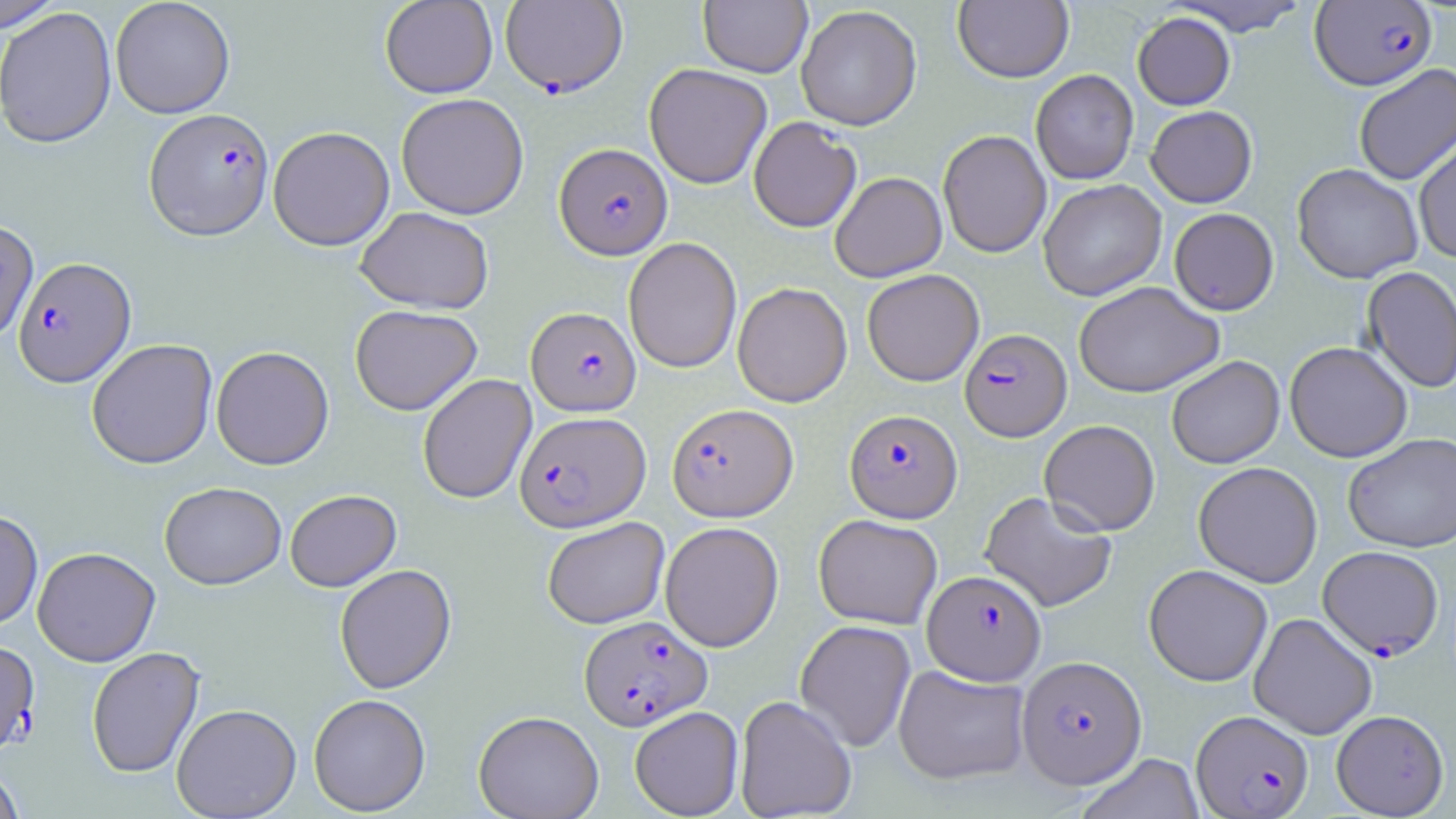

Summary:
  - Coordinate format: approximate bounding boxes as [x1, y1, x2, y2] in pixels
  - Uninfected red blood cell locations: [110, 0, 235, 119], [380, 0, 498, 98], [699, 0, 812, 77], [1166, 0, 1312, 36], [0, 1, 64, 32], [953, 1, 1074, 83], [0, 5, 117, 148], [796, 5, 922, 130], [1132, 11, 1236, 110], [644, 63, 772, 189], [1353, 65, 1456, 186], [1031, 69, 1139, 185], [396, 93, 529, 219], [1145, 105, 1257, 208], [748, 117, 862, 232], [268, 126, 395, 251], [937, 130, 1051, 258], [1414, 135, 1456, 264], [1292, 163, 1423, 284], [829, 171, 947, 282], [1038, 179, 1166, 301], [355, 206, 494, 314], [1169, 208, 1279, 315], [0, 219, 38, 343], [623, 237, 742, 374], [1362, 266, 1456, 393], [861, 269, 984, 386], [1073, 281, 1224, 398], [732, 282, 852, 407], [350, 304, 482, 415], [86, 338, 218, 469], [1284, 341, 1412, 462], [211, 346, 334, 470], [1166, 355, 1284, 469], [417, 373, 537, 504], [1039, 419, 1160, 535], [1343, 433, 1456, 552], [1193, 461, 1323, 587], [159, 481, 286, 589], [285, 489, 401, 591], [980, 490, 1117, 613], [0, 510, 42, 629], [813, 513, 943, 629], [542, 516, 670, 629], [660, 521, 784, 652], [32, 546, 160, 667], [334, 563, 456, 694], [1143, 564, 1273, 686], [1249, 613, 1377, 739], [795, 620, 916, 752], [86, 646, 205, 778], [893, 664, 1030, 785], [308, 693, 431, 815], [734, 695, 857, 819], [172, 703, 301, 818], [629, 705, 744, 818], [1331, 709, 1448, 818], [473, 710, 604, 819], [1075, 753, 1205, 819], [0, 764, 25, 819]
  - Plasmodium falciparum-infected red blood cell locations: [499, 0, 627, 97], [1310, 1, 1437, 91], [144, 108, 274, 240], [554, 143, 672, 259], [13, 256, 136, 387], [526, 306, 640, 416], [960, 328, 1071, 441], [667, 403, 798, 521], [845, 409, 962, 523], [515, 411, 651, 531], [1317, 545, 1443, 660], [923, 570, 1046, 684], [579, 615, 712, 730], [0, 640, 39, 754], [1017, 655, 1146, 788], [1191, 710, 1313, 818]
  - Slide-level diagnosis: Plasmodium falciparum
  - Magnification: 1000x
  - Preparation: thin blood film
  - Field of view: single
  - Modality: light microscopy
  - Image size: 1456×819 pixels
  - Stain: May-Grünwald-Giemsa